Classify this cell by malaria status.
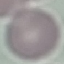
It is uninfected.

Summary:
  - Preparation: thin blood film
  - Capture: smartphone camera at the microscope eyepiece
  - Image type: automatically extracted cell patch, resized to 64 × 64 pixels
  - Stain: Giemsa